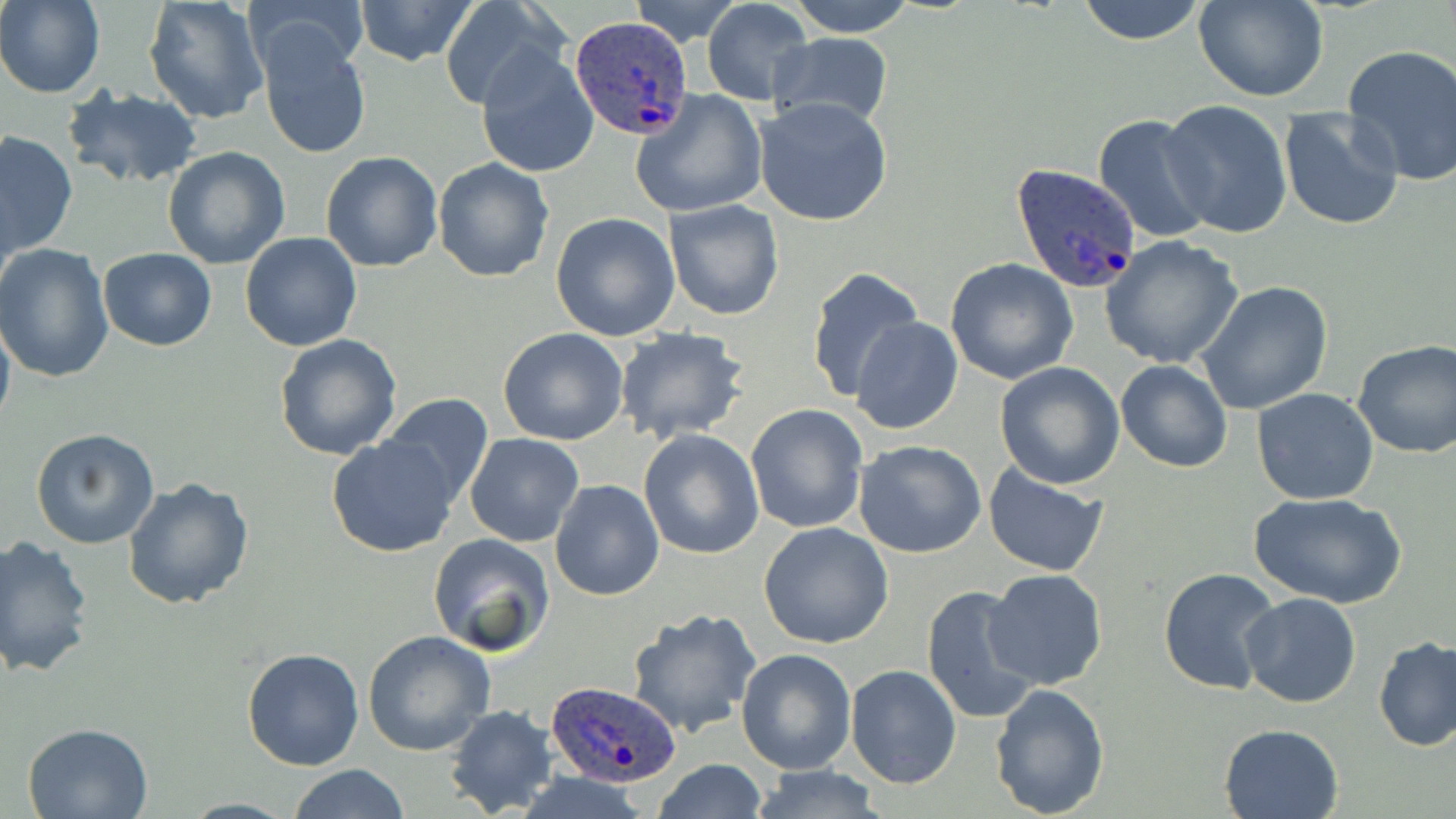

Summary:
  - Coordinate format: approximate bounding boxes as named x1/y1/x2/y2 corners in pixels
  - Uninfected red blood cell locations (subset): (x1=1, y1=0, x2=104, y2=98), (x1=143, y1=0, x2=270, y2=124), (x1=351, y1=0, x2=481, y2=67), (x1=627, y1=0, x2=741, y2=43), (x1=786, y1=0, x2=918, y2=38), (x1=1074, y1=0, x2=1211, y2=46), (x1=1193, y1=0, x2=1330, y2=102), (x1=246, y1=1, x2=368, y2=84), (x1=437, y1=1, x2=561, y2=108), (x1=701, y1=1, x2=812, y2=106), (x1=256, y1=28, x2=374, y2=159), (x1=767, y1=34, x2=892, y2=131), (x1=476, y1=42, x2=600, y2=178), (x1=1341, y1=44, x2=1456, y2=188), (x1=65, y1=86, x2=203, y2=188), (x1=631, y1=89, x2=767, y2=218), (x1=754, y1=96, x2=892, y2=227), (x1=1159, y1=100, x2=1293, y2=238), (x1=1277, y1=108, x2=1405, y2=230), (x1=0, y1=131, x2=77, y2=259), (x1=163, y1=146, x2=290, y2=267), (x1=321, y1=150, x2=444, y2=273), (x1=432, y1=157, x2=556, y2=283), (x1=663, y1=199, x2=784, y2=321), (x1=550, y1=212, x2=681, y2=341), (x1=239, y1=232, x2=361, y2=351), (x1=1101, y1=235, x2=1244, y2=370), (x1=1, y1=243, x2=117, y2=381), (x1=97, y1=248, x2=217, y2=350), (x1=945, y1=259, x2=1078, y2=385), (x1=807, y1=266, x2=926, y2=405), (x1=1195, y1=281, x2=1334, y2=415), (x1=0, y1=308, x2=15, y2=438), (x1=849, y1=316, x2=965, y2=436), (x1=614, y1=327, x2=748, y2=443), (x1=499, y1=328, x2=629, y2=445), (x1=274, y1=334, x2=403, y2=460), (x1=1352, y1=340, x2=1456, y2=458), (x1=1116, y1=359, x2=1233, y2=472), (x1=995, y1=362, x2=1126, y2=489), (x1=1252, y1=388, x2=1379, y2=506), (x1=378, y1=393, x2=494, y2=507), (x1=746, y1=404, x2=868, y2=534), (x1=31, y1=428, x2=160, y2=549), (x1=639, y1=430, x2=764, y2=560), (x1=464, y1=433, x2=583, y2=546), (x1=327, y1=435, x2=460, y2=557), (x1=854, y1=439, x2=987, y2=557), (x1=984, y1=464, x2=1109, y2=579), (x1=122, y1=476, x2=256, y2=612), (x1=551, y1=480, x2=665, y2=602), (x1=1248, y1=491, x2=1408, y2=609), (x1=758, y1=522, x2=894, y2=648), (x1=427, y1=532, x2=556, y2=656), (x1=0, y1=536, x2=96, y2=678), (x1=1158, y1=566, x2=1283, y2=694), (x1=984, y1=568, x2=1109, y2=691), (x1=920, y1=583, x2=1044, y2=726), (x1=1241, y1=593, x2=1362, y2=709), (x1=626, y1=608, x2=764, y2=739), (x1=362, y1=631, x2=496, y2=756), (x1=1373, y1=635, x2=1456, y2=752), (x1=242, y1=646, x2=363, y2=771), (x1=735, y1=647, x2=857, y2=775), (x1=846, y1=664, x2=961, y2=788), (x1=989, y1=683, x2=1110, y2=816), (x1=445, y1=704, x2=560, y2=818), (x1=23, y1=722, x2=154, y2=818), (x1=1219, y1=722, x2=1346, y2=819), (x1=653, y1=758, x2=767, y2=819), (x1=287, y1=765, x2=409, y2=819), (x1=747, y1=765, x2=891, y2=818)
  - Plasmodium ovale-infected red blood cell locations (subset): (x1=571, y1=16, x2=693, y2=139), (x1=1009, y1=163, x2=1141, y2=295), (x1=544, y1=679, x2=683, y2=788)
  - Slide-level diagnosis: Plasmodium ovale
  - Preparation: thin blood film
  - Magnification: 1000x
  - Modality: optical microscopy
  - Stain: May-Grünwald-Giemsa
  - Field of view: one of a larger specimen
  - Image size: 1456×819 pixels